Mark where cells are.
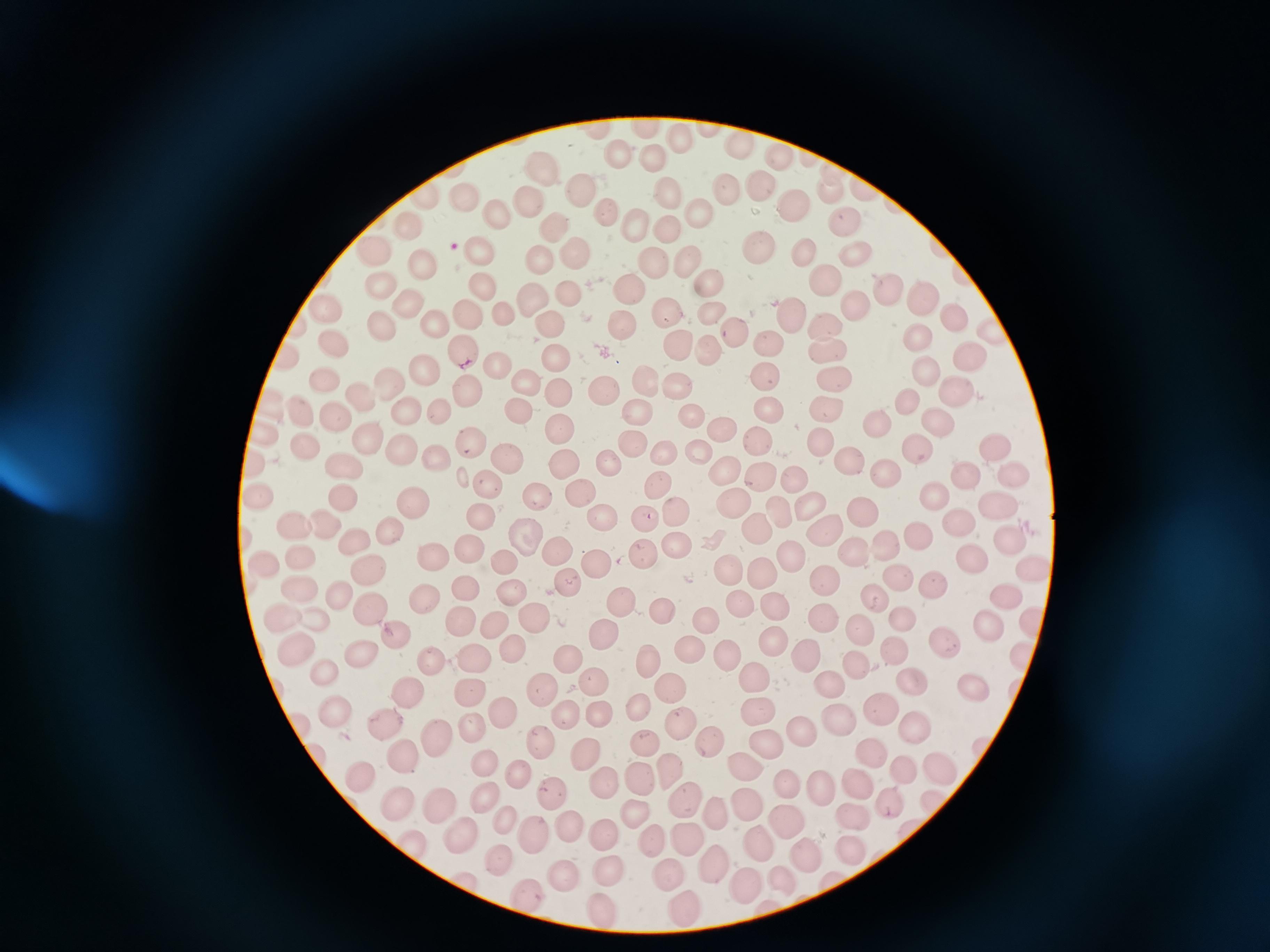

Approximate centers as (x, y) in pixels.
Cells: (677, 141), (741, 145), (620, 152), (652, 157), (781, 161), (537, 170), (832, 170), (576, 185), (726, 185), (755, 190), (670, 192), (833, 192), (467, 195), (428, 197), (526, 203), (795, 207), (606, 211), (703, 212), (495, 214), (635, 222), (408, 224), (846, 225), (557, 226), (666, 227), (760, 246), (376, 248), (478, 251), (575, 252), (852, 252), (803, 253), (538, 256), (653, 263), (421, 264), (692, 264), (821, 280), (709, 281), (381, 282), (484, 285), (633, 287), (884, 288), (918, 293), (568, 295), (533, 301), (852, 302), (404, 304), (325, 307), (665, 308), (712, 310), (790, 315), (953, 315), (501, 316), (471, 317), (550, 322), (619, 322), (380, 324), (436, 325), (823, 325), (732, 332), (919, 336), (770, 342), (333, 344), (679, 344), (710, 346), (825, 347), (462, 351), (560, 354), (968, 358), (501, 363), (426, 369), (929, 370), (765, 376), (832, 378), (324, 380), (529, 380), (645, 380), (390, 381), (678, 385), (602, 388), (466, 390), (558, 391), (958, 394), (362, 400), (910, 400), (520, 407), (441, 408), (824, 408), (767, 409), (638, 410), (404, 411), (301, 412), (692, 412), (336, 416), (874, 419), (937, 424), (720, 429), (563, 430), (267, 435), (367, 436), (471, 437), (820, 437), (758, 440), (631, 442), (306, 447), (994, 448), (398, 449), (918, 449), (698, 450), (665, 453), (504, 456), (435, 457), (562, 461), (849, 462), (256, 463), (345, 464), (608, 467), (725, 468), (1013, 474), (887, 475), (960, 475), (761, 476), (485, 483), (661, 487), (582, 490), (262, 495), (533, 495), (933, 495), (343, 496), (731, 503), (415, 506), (809, 508), (994, 508), (865, 509), (478, 512), (675, 514), (599, 515), (645, 520), (326, 521), (296, 524), (756, 527), (960, 527), (390, 532), (822, 533), (917, 534), (523, 538), (360, 539), (1010, 540), (885, 545), (677, 546), (470, 548), (857, 548), (555, 549), (642, 554), (301, 556), (439, 556), (791, 557), (969, 557), (502, 561), (596, 563), (1030, 563), (267, 566), (727, 567), (759, 570), (373, 571), (900, 580), (825, 581), (567, 583), (464, 585), (933, 586), (307, 592), (510, 593), (1006, 594), (343, 597), (872, 598), (423, 602), (621, 603), (737, 603), (368, 604), (779, 606), (281, 614), (662, 615), (534, 616), (820, 616), (904, 617), (706, 618), (990, 620), (460, 621), (494, 626), (858, 628), (393, 634), (605, 634), (773, 638), (940, 640), (892, 644), (295, 646), (689, 647), (359, 651), (804, 651), (725, 655), (568, 657), (432, 658), (473, 658), (645, 659), (1021, 659), (855, 666), (324, 672), (749, 673), (827, 680), (598, 681), (913, 681), (970, 681), (670, 686), (406, 687), (543, 687), (468, 694), (884, 703), (640, 705), (335, 709), (499, 709), (754, 709), (566, 714), (603, 715), (835, 720), (388, 721), (678, 721), (470, 722), (911, 729), (799, 730), (436, 735), (538, 740), (711, 742), (761, 742), (643, 744), (869, 751), (402, 752), (584, 752), (485, 759), (744, 764), (668, 766), (939, 767), (905, 768), (520, 770), (357, 771), (602, 781), (640, 781), (855, 782), (784, 783), (820, 786), (554, 789), (485, 795), (681, 797), (887, 797), (744, 799), (929, 801), (398, 803), (441, 807), (634, 811), (712, 811), (853, 811), (785, 820), (507, 822), (571, 824), (460, 833), (600, 834), (533, 835), (689, 840), (655, 842), (413, 844), (759, 844), (850, 846), (809, 853), (498, 854), (717, 862), (609, 871), (671, 874), (779, 875), (565, 879), (746, 887), (521, 892), (685, 904), (600, 906).

field_of_view: single
preparation: thin smear
capture: smartphone camera at the microscope eyepiece
image_size: 1270×952 pixels
stain: Giemsa